Classify this cell by malaria status.
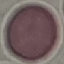

Uninfected.

stain = Giemsa
preparation = thin smear
image type = cell patch, automatically extracted from a larger field of view and resized to 64 × 64 pixels
capture = smartphone through the microscope eyepiece